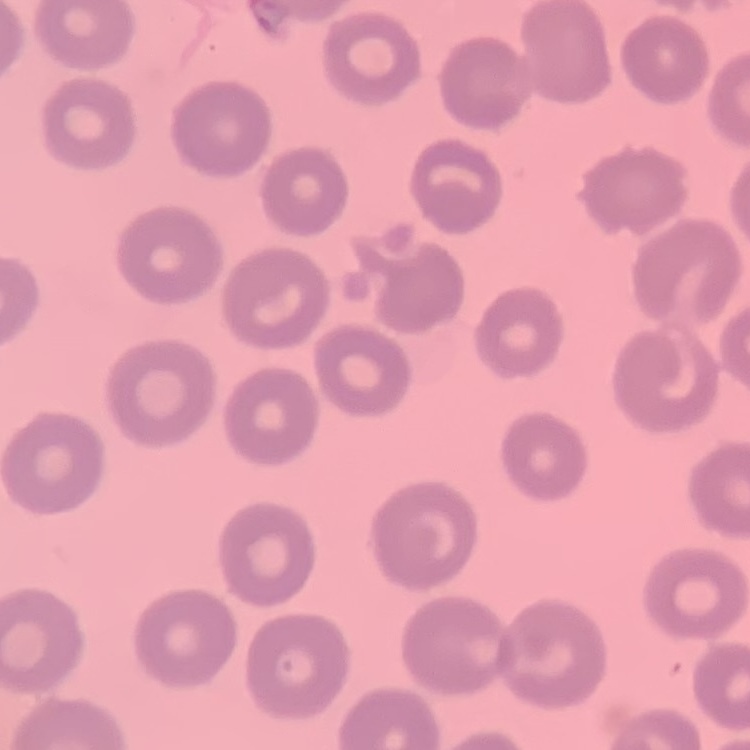
The red blood cells show no rouleaux formation. Field's or Giemsa stain. Thin peripheral smear. One tile cut from a larger photomicrograph.